Assess the morphology of the erythrocytes.
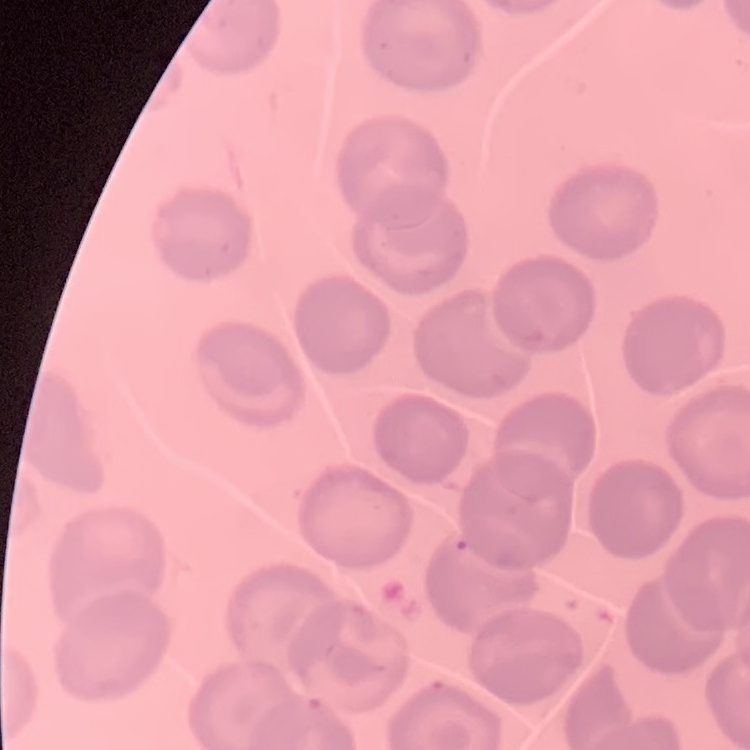

No rouleaux formation.

Summary:
  - Preparation: thin peripheral smear
  - Image type: square crop of a larger photomicrograph
  - Stain: Field's or Giemsa